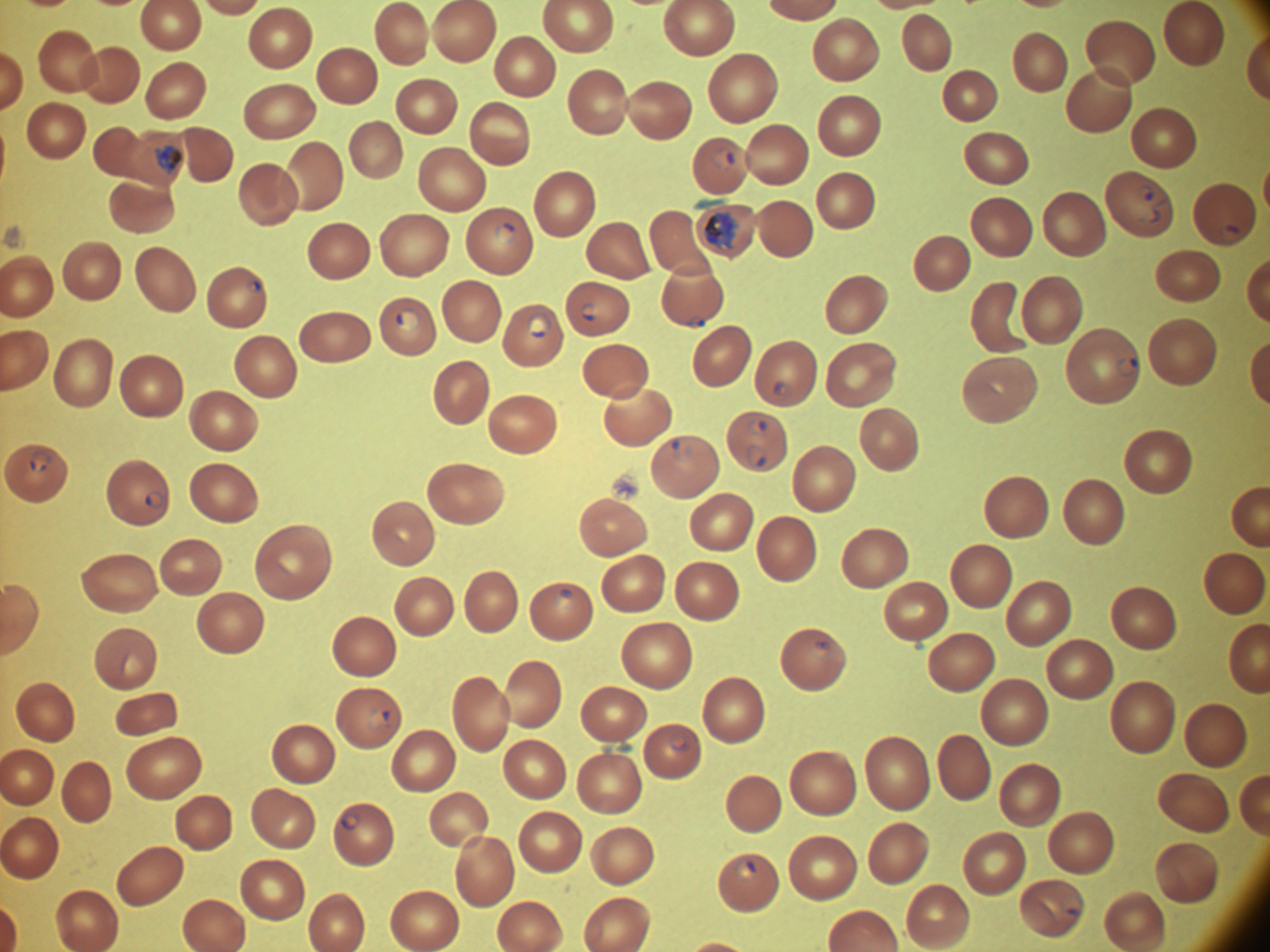
life-cycle stages among the annotated parasites = ring form, trophozoite
microscope = Leica DM2000 with built-in camera
ring form locations = approximate bounding boxes as (x1,y1)-(x2,y2) corner pairs in pixels, from the source annotation, which is not necessarily exhaustive: (710,147)-(735,169), (1139,183)-(1167,224), (495,222)-(517,244), (1221,224)-(1243,243), (246,278)-(262,293), (581,303)-(597,321), (395,308)-(421,332), (526,311)-(552,338), (689,315)-(708,330), (1116,357)-(1138,379), (773,380)-(793,400), (748,418)-(769,436), (671,438)-(694,461), (746,444)-(768,468), (30,451)-(52,473), (146,490)-(166,508), (810,641)-(831,658), (366,710)-(392,731), (670,732)-(692,752), (341,814)-(361,830), (732,857)-(758,884), (1060,895)-(1082,916)
image size = 1270×952 pixels
trophozoite locations = approximate bounding boxes as (x1,y1)-(x2,y2) corner pairs in pixels, from the source annotation, which is not necessarily exhaustive: (156,144)-(184,176), (704,211)-(741,252)
species = Plasmodium falciparum
field of view = one from this slide
preparation = thin blood film
stain = Giemsa
magnification = 100x